State the blood parasite species.
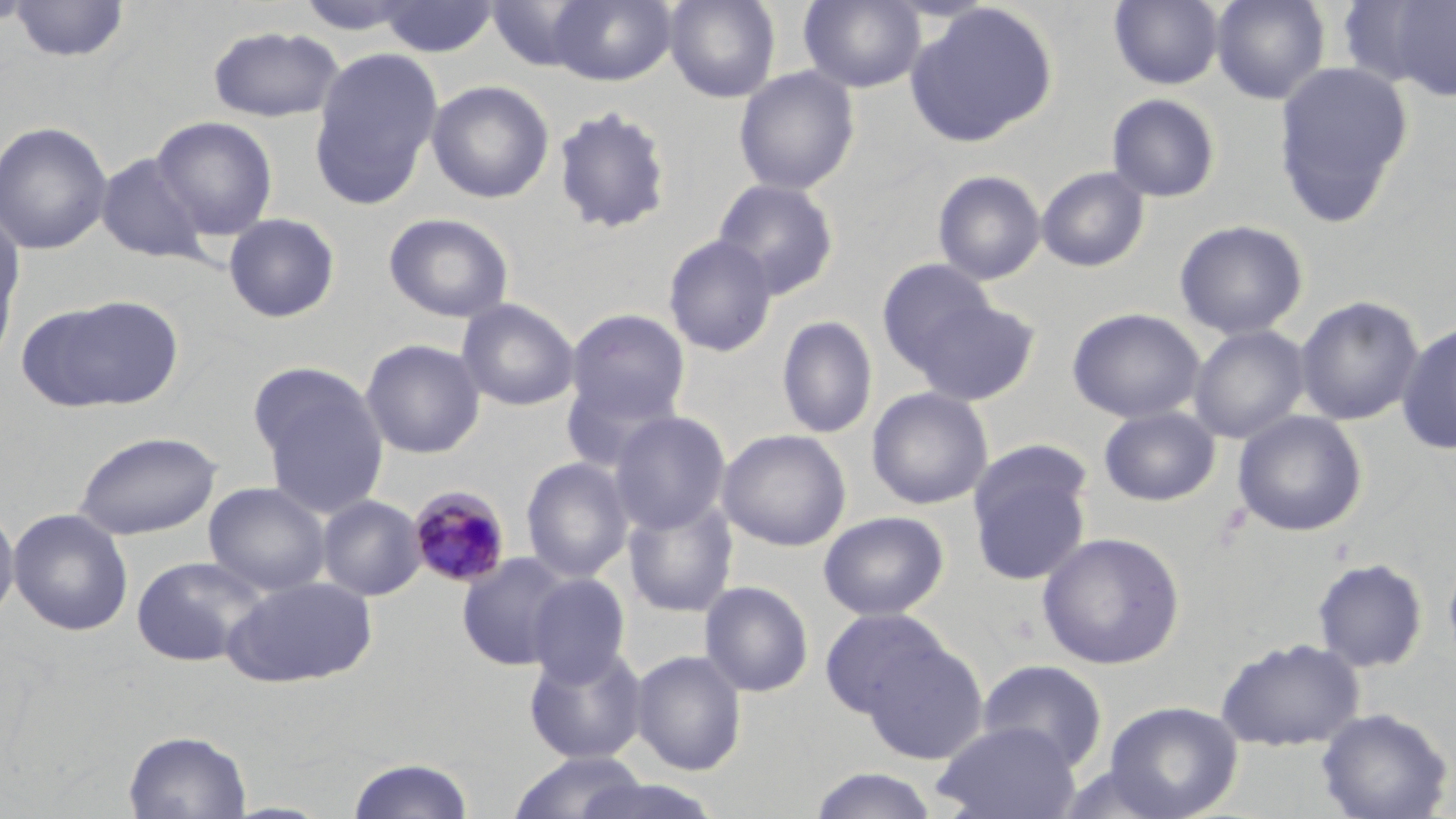

Plasmodium malariae.

uninfected red blood cell locations = approximate bounding boxes as (x1,y1)-(x2,y2) corner pairs in pixels: (0,0)-(35,32), (548,0)-(677,86), (664,0)-(781,103), (799,0)-(926,92), (1109,0)-(1224,90), (1211,0)-(1330,104), (1348,0)-(1456,100), (9,1)-(131,63), (375,1)-(499,58), (486,1)-(599,72), (905,2)-(1058,147), (207,25)-(345,123), (309,47)-(443,208), (1273,60)-(1414,223), (733,66)-(860,195), (427,80)-(554,203), (1106,93)-(1221,202), (552,105)-(675,235), (151,115)-(278,240), (0,121)-(113,255), (95,152)-(211,264), (1036,166)-(1150,272), (932,170)-(1046,285), (712,178)-(840,299), (383,212)-(515,323), (0,213)-(25,364), (223,213)-(341,323), (1174,219)-(1309,339), (663,234)-(779,358), (877,258)-(996,369), (32,294)-(185,412), (1295,295)-(1425,426), (909,296)-(1040,406), (456,299)-(580,411), (1067,307)-(1205,424), (565,308)-(691,427), (776,315)-(878,439), (1396,321)-(1456,456), (1188,325)-(1310,444), (360,339)-(485,459), (252,368)-(389,518), (560,373)-(681,474), (866,387)-(993,510), (1099,407)-(1220,506), (1232,409)-(1368,537), (609,410)-(731,534), (717,429)-(851,551), (72,430)-(223,541), (967,446)-(1094,587), (520,456)-(634,583), (203,482)-(331,596), (317,495)-(426,601), (622,496)-(739,618), (0,502)-(19,627), (7,508)-(134,636), (818,511)-(949,620), (1037,531)-(1185,669), (457,553)-(573,671), (130,554)-(270,668), (1442,555)-(1456,670), (1312,558)-(1428,673), (525,574)-(630,686), (221,575)-(378,689), (699,580)-(814,698), (819,608)-(950,721), (1216,636)-(1364,751), (860,639)-(989,764), (524,643)-(649,764), (630,649)-(747,776), (976,658)-(1108,771), (1104,700)-(1243,819), (1315,707)-(1454,819), (932,720)-(1081,819), (124,729)-(252,818), (508,750)-(653,819), (345,757)-(475,818), (808,768)-(940,818), (566,774)-(724,819)
stain = May-Grünwald-Giemsa
Plasmodium malariae-infected red blood cell locations = approximate bounding boxes as (x1,y1)-(x2,y2) corner pairs in pixels: (408,486)-(512,589)
image size = 1456×819 pixels
field of view = single
magnification = 1000x
modality = optical microscopy
preparation = thin blood film